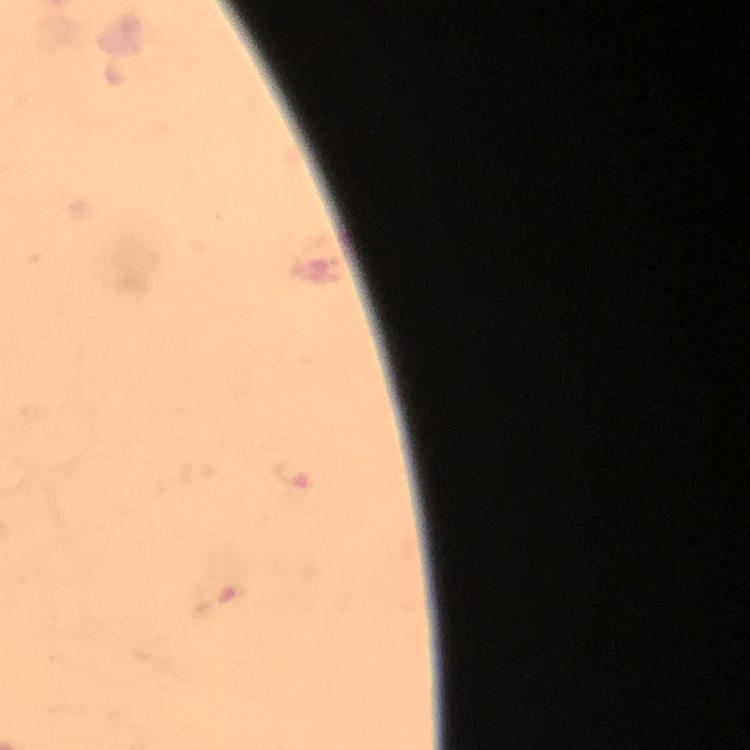
{
  "preparation": "thick blood smear",
  "cropped_from": "a single field of view",
  "image_size": "750×750 pixels",
  "plasmodium_parasite_locations": "approximate object centers, in pixels from the top-left corner: (x=292, y=476)",
  "capture": "smartphone mounted on the microscope",
  "stain": "Giemsa",
  "immersion_oil": "used",
  "magnification": "100x",
  "context": "from a diagnostic examination for malaria"
}